Classify this cell by malaria status.
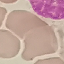

It is uninfected.

image type = automatically extracted cell patch, resized to 64 × 64 pixels
stain = Giemsa
capture = smartphone camera at the microscope eyepiece
preparation = thin blood smear